Assess this cell for malaria.
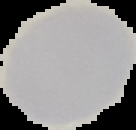

It is uninfected.

image_size: 136×130 pixels
image_type: segmented cell region on a black background
preparation: thin blood smear